Locate every Plasmodium parasite and every leukocyte.
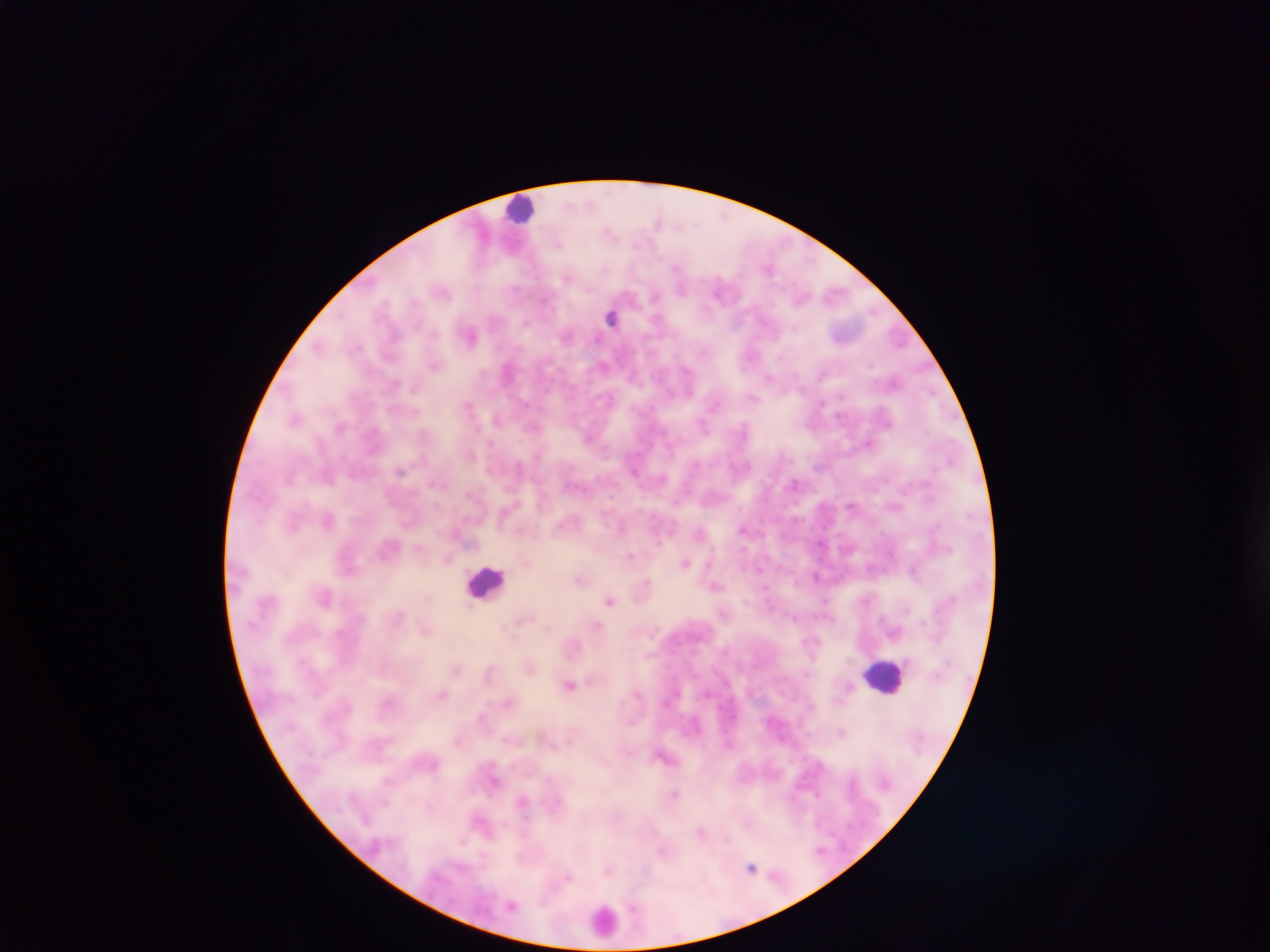

Approximate centers as {x, y} in pixels.
Plasmodium parasites: {612, 315}, {470, 334}, {566, 334}, {509, 369}, {769, 378}, {895, 381}, {468, 406}, {295, 418}, {497, 418}, {341, 427}, {869, 443}, {401, 470}, {796, 484}, {328, 518}, {743, 528}, {702, 533}, {630, 556}, {448, 558}, {685, 562}, {816, 576}, {580, 579}, {645, 584}, {716, 586}, {325, 597}, {610, 600}, {521, 619}, {598, 627}, {426, 630}, {530, 667}, {457, 669}, {569, 685}, {442, 695}, {508, 701}, {482, 717}, {842, 732}, {457, 741}, {665, 756}, {675, 795}, {523, 802}, {702, 832}, {820, 851}, {663, 852}, {752, 868}, {608, 869}, {568, 876}, {511, 905}.
Leukocytes: {521, 210}, {485, 583}, {886, 675}, {605, 920}.

Summary:
  - Country: Ghana
  - Preparation: thick blood film
  - Capture: mobile-phone photograph through a microscope
  - Field of view: single
  - Image size: 1270×952 pixels